Identify the preparation type.
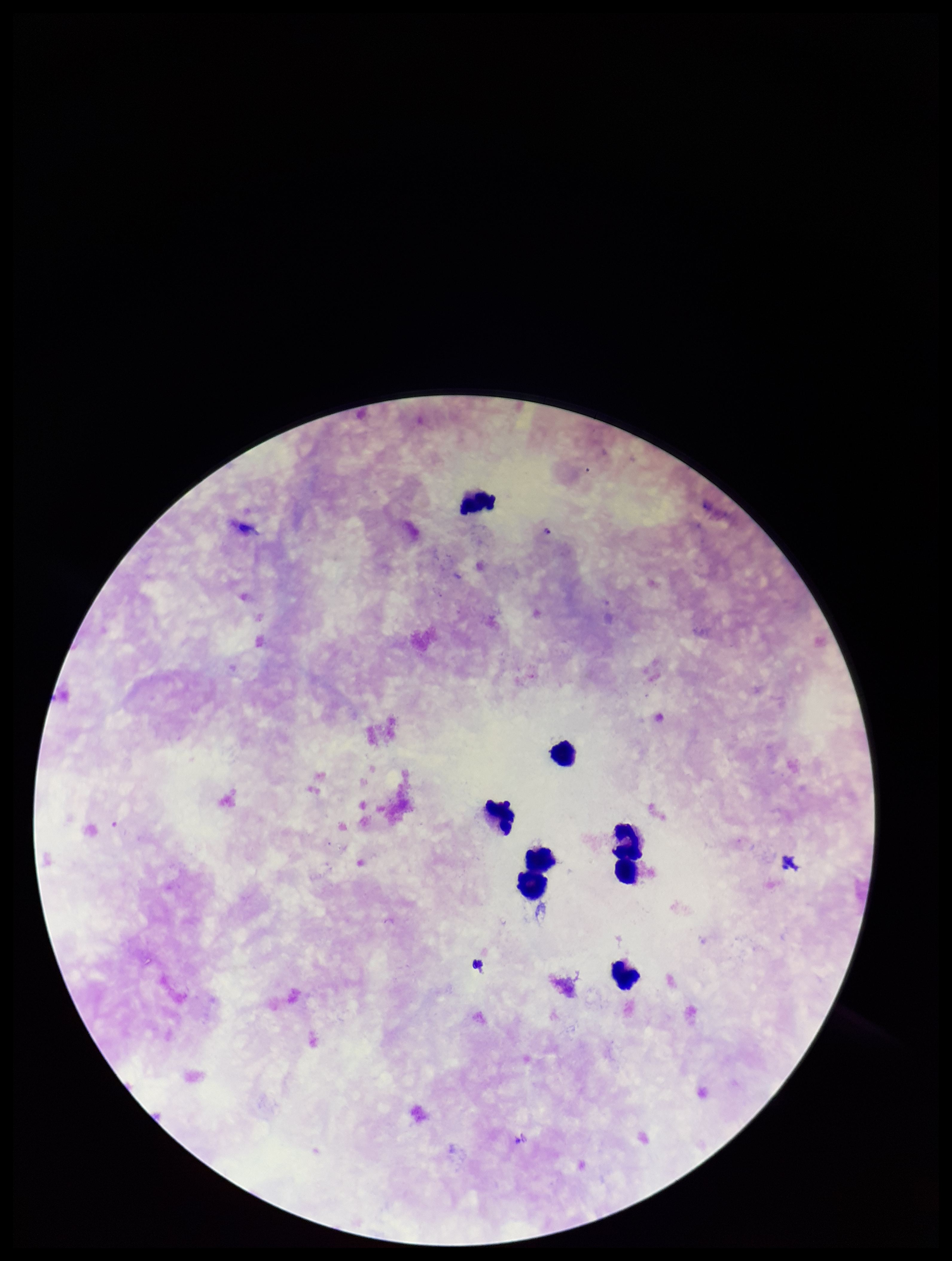

Thick.

Summary:
  - Patient malaria status: infected
  - Species reported for this patient: Plasmodium falciparum
  - Stain: Giemsa
  - Image size: 952×1261 pixels
  - Leukocyte count: 8
  - Field of view: single
  - Parasite count: 1
  - Plasmodium parasites: identified
  - Capture: smartphone photograph through the microscope eyepiece